Evaluate for Plasmodium parasites.
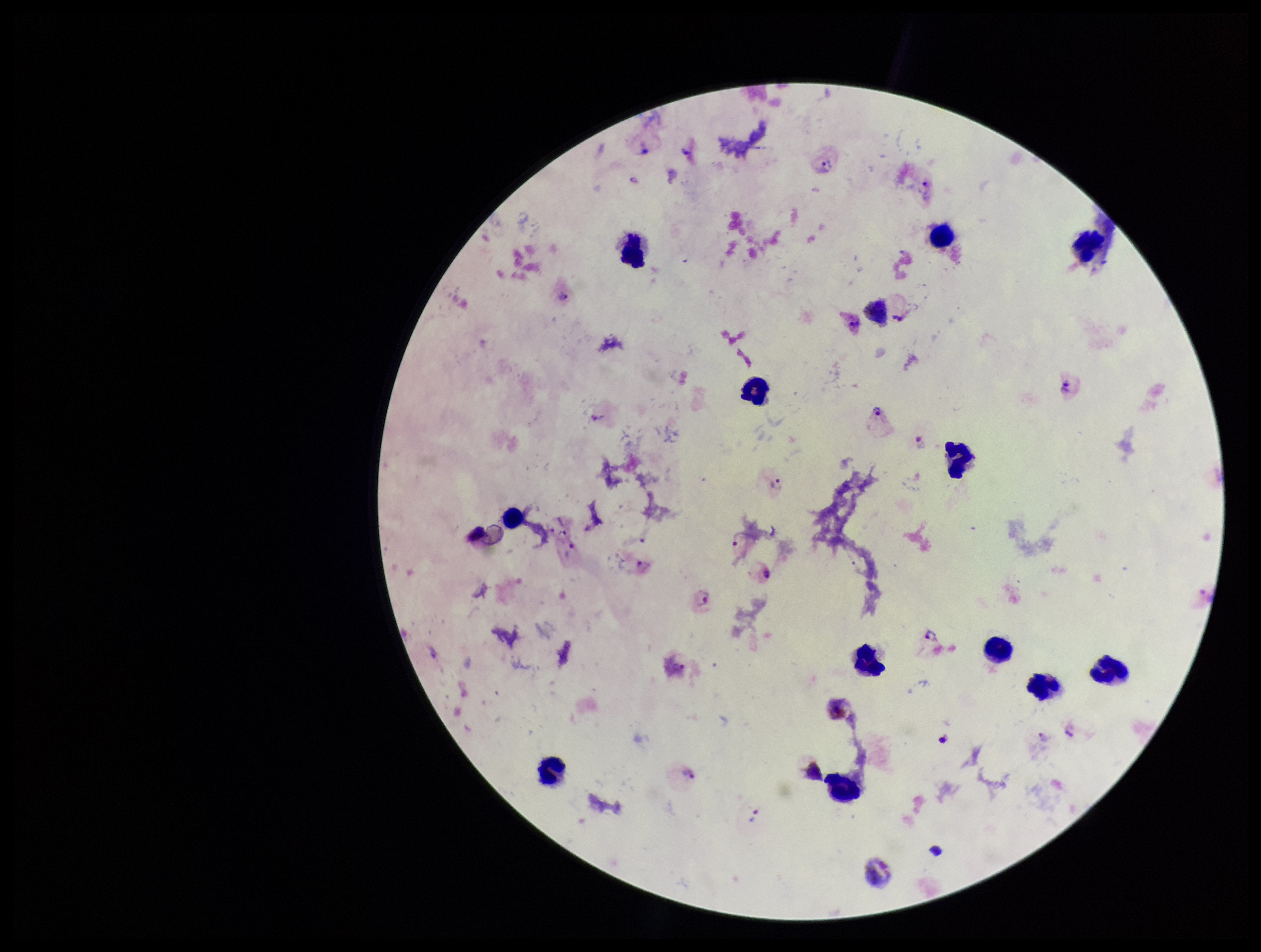

Seen.

species reported for this patient = Plasmodium vivax
field of view = single
preparation = thick
capture = smartphone photograph through the microscope eyepiece
parasite count = 8
stain = Giemsa
patient malaria status = infected
leukocyte count = 13
image size = 1261×952 pixels